Assess this cell for malaria.
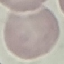
It is uninfected.

{
  "stain": "Giemsa",
  "capture": "smartphone camera at the microscope eyepiece",
  "preparation": "thin blood smear",
  "image_type": "cell patch, automatically extracted from a larger field of view and resized to 64 × 64 pixels"
}